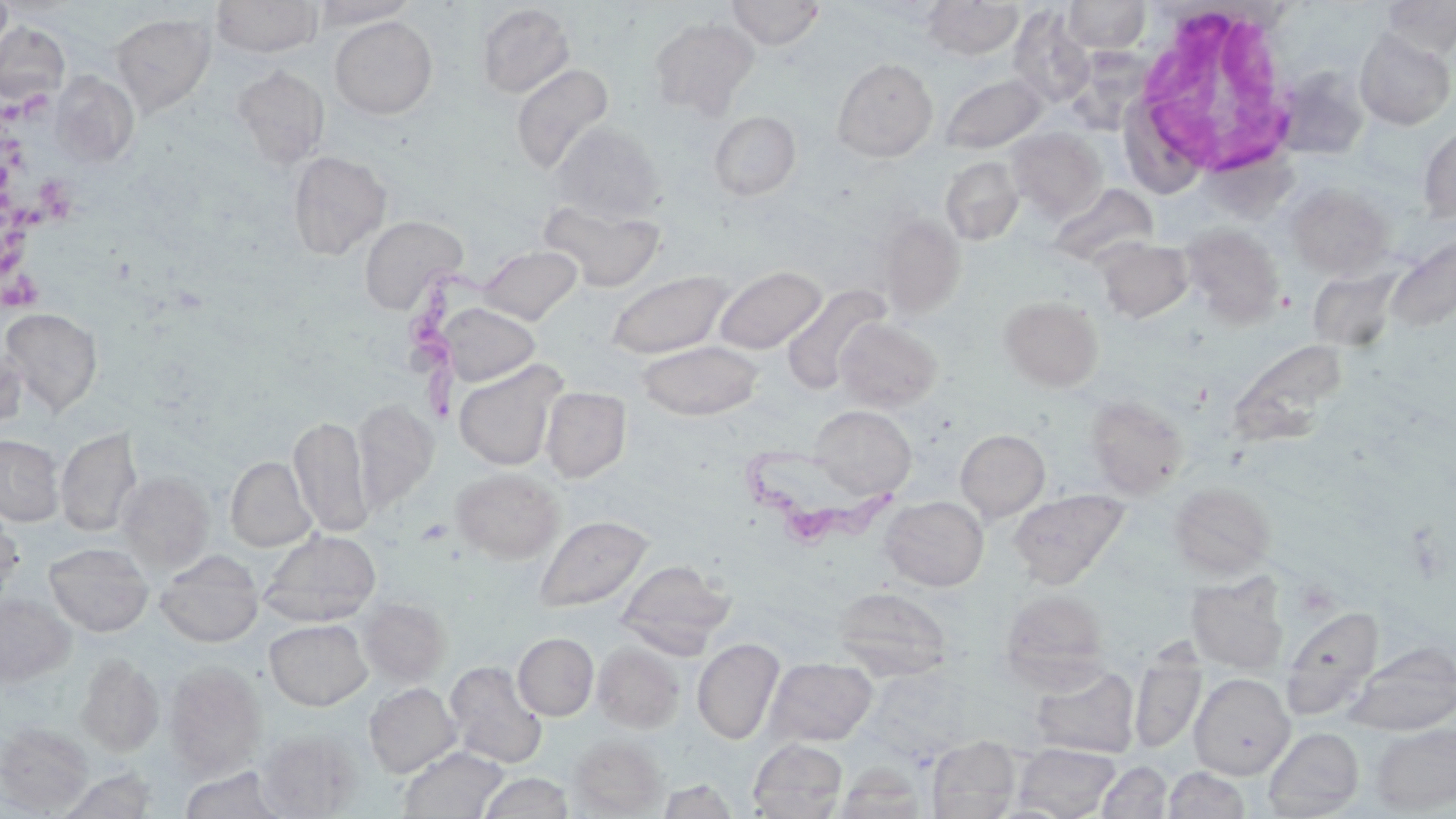

Summary:
  - Coordinate format: approximate bounding boxes as [x1, y1, x2, y2] in pixels
  - Uninfected red blood cell locations: [0, 0, 14, 63], [211, 0, 322, 58], [309, 0, 421, 27], [727, 0, 825, 49], [922, 0, 1023, 60], [1062, 0, 1150, 54], [1381, 0, 1456, 58], [476, 3, 575, 99], [1007, 5, 1095, 109], [111, 12, 216, 116], [329, 16, 437, 119], [649, 17, 758, 118], [0, 22, 70, 106], [1354, 29, 1455, 130], [1067, 32, 1151, 134], [833, 57, 938, 161], [511, 63, 615, 176], [232, 64, 330, 168], [1274, 66, 1370, 159], [50, 72, 140, 167], [939, 72, 1048, 154], [709, 111, 801, 201], [550, 122, 664, 225], [1418, 123, 1456, 224], [1007, 127, 1106, 221], [288, 150, 391, 259], [940, 156, 1024, 245], [1046, 183, 1157, 268], [1285, 183, 1394, 280], [540, 200, 665, 293], [879, 213, 965, 319], [359, 215, 467, 314], [1180, 222, 1284, 326], [1096, 238, 1194, 323], [480, 245, 582, 325], [714, 265, 827, 354], [606, 270, 733, 360], [783, 284, 891, 395], [999, 296, 1103, 391], [438, 303, 540, 386], [1, 308, 103, 416], [834, 317, 942, 412], [638, 340, 764, 420], [1230, 340, 1348, 444], [0, 341, 26, 435], [453, 360, 566, 471], [540, 387, 630, 482], [1085, 394, 1189, 498], [352, 398, 438, 510], [809, 405, 916, 500], [288, 416, 372, 536], [56, 426, 143, 537], [955, 429, 1050, 522], [0, 434, 64, 526], [225, 457, 316, 552], [451, 467, 563, 564], [116, 471, 214, 573], [1169, 481, 1275, 578], [1008, 488, 1129, 588], [881, 495, 988, 591], [0, 508, 24, 602], [535, 515, 652, 612], [260, 529, 380, 627], [45, 542, 153, 636], [156, 551, 262, 647], [618, 559, 736, 653], [1186, 575, 1288, 675], [831, 586, 952, 681], [1000, 589, 1109, 687], [0, 592, 75, 686], [360, 597, 450, 685], [1280, 604, 1384, 721], [265, 619, 372, 710], [513, 633, 599, 720], [692, 638, 784, 745], [592, 642, 684, 733], [1346, 642, 1456, 734], [1130, 649, 1205, 755], [76, 653, 164, 757], [765, 657, 877, 747], [444, 660, 548, 769], [163, 662, 266, 778], [1030, 664, 1140, 758], [1189, 673, 1294, 779], [364, 682, 460, 777], [1, 722, 94, 814], [1371, 723, 1456, 813], [1263, 727, 1364, 818], [258, 733, 358, 816], [569, 735, 667, 816], [927, 735, 1021, 818], [748, 738, 848, 818], [1014, 742, 1120, 819], [398, 746, 510, 818], [1097, 760, 1173, 818], [834, 764, 925, 818], [178, 766, 290, 819], [1164, 766, 1251, 819], [57, 769, 158, 818], [478, 772, 574, 819], [657, 778, 739, 819]
  - Trypanosoma brucei locations: [409, 249, 542, 424], [749, 442, 900, 552]
  - Platelet locations: [0, 81, 53, 132], [1, 134, 45, 193], [36, 175, 85, 222], [0, 193, 53, 277], [2, 270, 45, 322]
  - White blood cell locations: [1131, 2, 1301, 180]
  - Slide-level diagnosis: Trypanosoma brucei
  - Stain: May-Grünwald-Giemsa
  - Image size: 1456×819 pixels
  - Field of view: single
  - Magnification: 1000x
  - Modality: light microscopy
  - Preparation: thin blood film